Comment on the background quality.
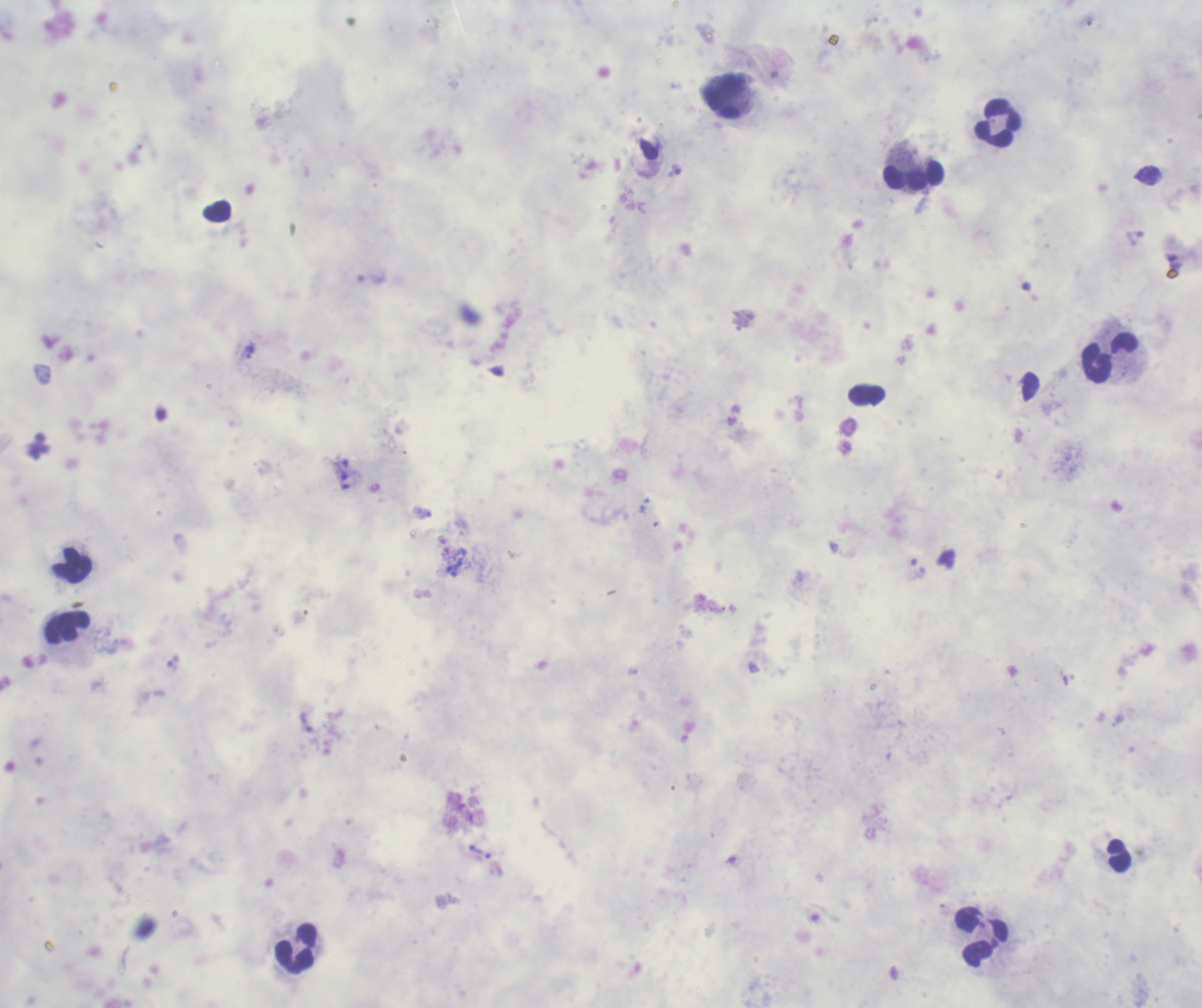

It is poor.

coordinate format = approximate object centers, in pixels from the top-left corner
leukocyte locations = (x=725, y=96), (x=999, y=123), (x=914, y=177), (x=1112, y=357), (x=71, y=564), (x=67, y=628), (x=981, y=938), (x=296, y=948)
trophozoite locations = (x=250, y=351), (x=645, y=506), (x=919, y=568), (x=307, y=723), (x=480, y=852)
preparation = thick blood film
result = malaria parasites detected
magnification = 100x
field of view = single
image size = 1202×1008 pixels
context = previously used in an actual diagnosis
stain = Romanowsky